Point out each Plasmodium parasite.
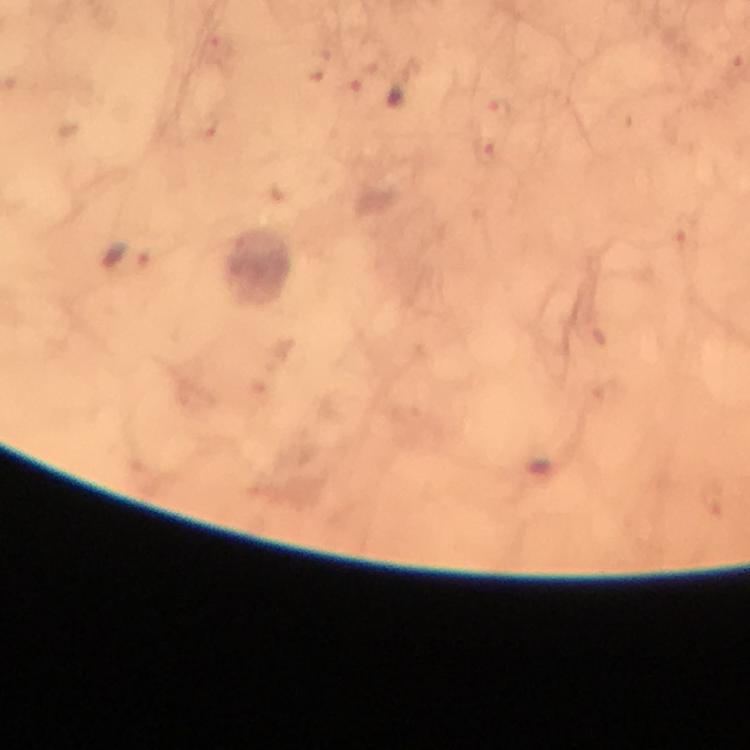
Approximate centers as [x, y] in pixels.
Plasmodium parasites: [129, 256].

{
  "preparation": "thick blood film",
  "magnification": "100x",
  "immersion_oil": "used",
  "capture": "smartphone photograph through a microscope",
  "stain": "Giemsa",
  "image_size": "750×750 pixels",
  "cropped_from": "a single field of view",
  "context": "from a malaria diagnostic workup"
}